Name the blood parasite species.
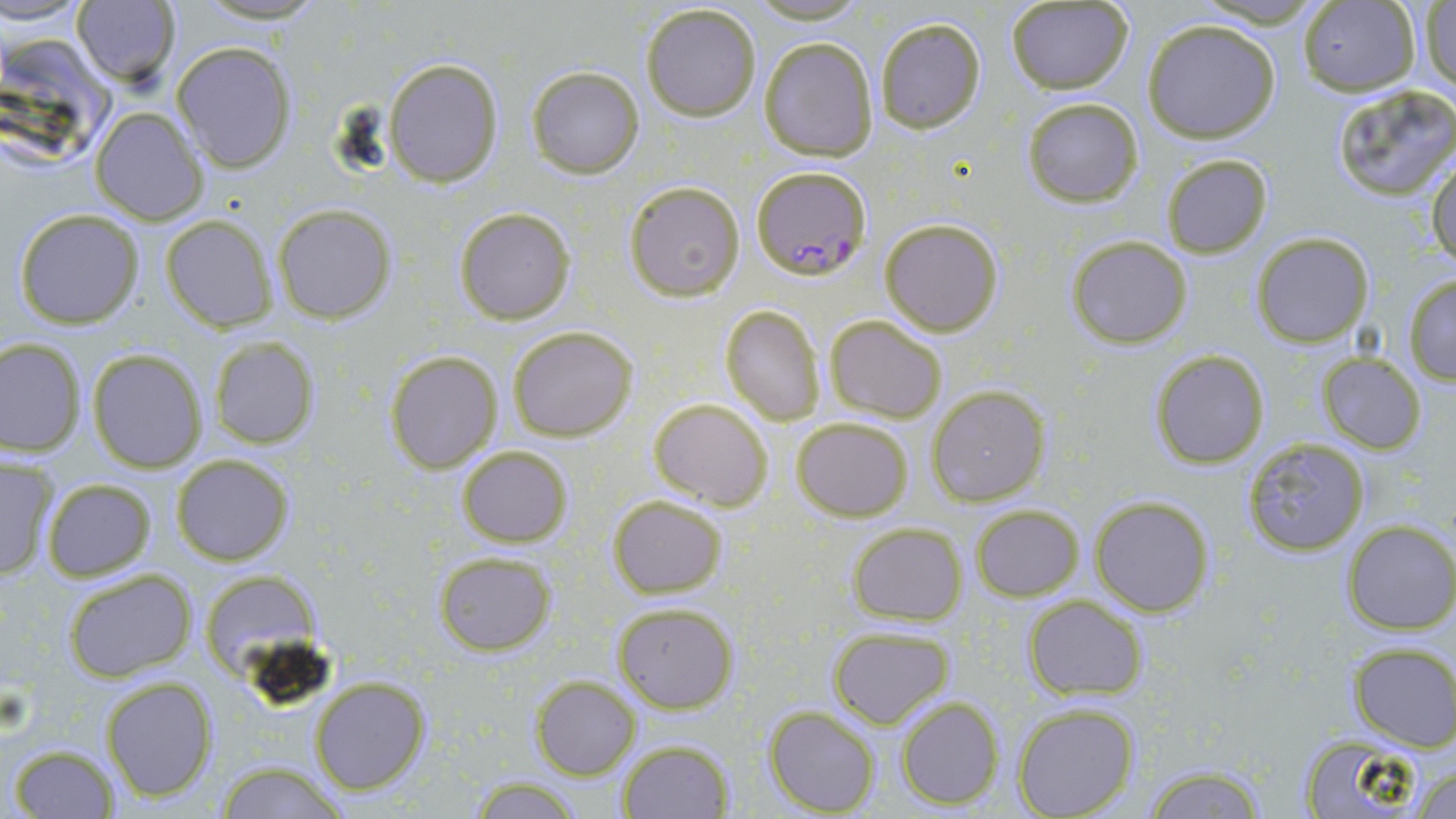
Plasmodium falciparum.

image_size: 1456×819 pixels
plasmodium_falciparum_infected_red_blood_cell_locations: 'approximate bounding boxes as named x1/y1/x2/y2 corners in pixels: (x1=749, y1=166, x2=870, y2=280)'
magnification: 1000x
preparation: thin blood smear
field_of_view: single
uninfected_red_blood_cell_locations: 'approximate bounding boxes as named x1/y1/x2/y2 corners in pixels: (x1=2, y1=0, x2=91, y2=29), (x1=186, y1=0, x2=338, y2=25), (x1=71, y1=1, x2=180, y2=87), (x1=1004, y1=1, x2=1134, y2=95), (x1=1296, y1=1, x2=1420, y2=95), (x1=1419, y1=3, x2=1456, y2=94), (x1=639, y1=4, x2=762, y2=120), (x1=875, y1=17, x2=988, y2=133), (x1=1142, y1=19, x2=1280, y2=144), (x1=0, y1=33, x2=118, y2=175), (x1=760, y1=37, x2=878, y2=163), (x1=170, y1=41, x2=297, y2=173), (x1=384, y1=57, x2=504, y2=186), (x1=526, y1=65, x2=645, y2=179), (x1=1329, y1=84, x2=1456, y2=202), (x1=1021, y1=98, x2=1142, y2=207), (x1=91, y1=107, x2=209, y2=225), (x1=1160, y1=154, x2=1273, y2=259), (x1=1430, y1=155, x2=1455, y2=270), (x1=623, y1=181, x2=745, y2=300), (x1=272, y1=204, x2=396, y2=324), (x1=453, y1=205, x2=576, y2=325), (x1=13, y1=207, x2=145, y2=330), (x1=161, y1=214, x2=278, y2=332), (x1=879, y1=217, x2=1004, y2=336), (x1=1252, y1=233, x2=1373, y2=348), (x1=1067, y1=237, x2=1192, y2=350), (x1=1402, y1=274, x2=1456, y2=384), (x1=720, y1=305, x2=825, y2=425), (x1=825, y1=315, x2=947, y2=422), (x1=506, y1=325, x2=638, y2=442), (x1=208, y1=335, x2=319, y2=449), (x1=0, y1=336, x2=86, y2=457), (x1=86, y1=348, x2=209, y2=472), (x1=384, y1=348, x2=503, y2=473), (x1=1148, y1=349, x2=1270, y2=469), (x1=1315, y1=354, x2=1427, y2=453), (x1=927, y1=385, x2=1049, y2=507), (x1=648, y1=398, x2=774, y2=510), (x1=792, y1=416, x2=912, y2=521), (x1=1242, y1=436, x2=1373, y2=558), (x1=458, y1=446, x2=573, y2=546), (x1=172, y1=454, x2=293, y2=566), (x1=0, y1=455, x2=59, y2=581), (x1=42, y1=479, x2=156, y2=580), (x1=1090, y1=494, x2=1214, y2=616), (x1=608, y1=495, x2=727, y2=598), (x1=971, y1=504, x2=1083, y2=601), (x1=1341, y1=520, x2=1456, y2=634), (x1=846, y1=522, x2=967, y2=626), (x1=433, y1=551, x2=556, y2=657), (x1=61, y1=568, x2=197, y2=683), (x1=208, y1=569, x2=320, y2=686), (x1=1022, y1=595, x2=1148, y2=700), (x1=614, y1=602, x2=739, y2=713), (x1=826, y1=626, x2=956, y2=728), (x1=1346, y1=645, x2=1456, y2=751), (x1=100, y1=675, x2=217, y2=802), (x1=530, y1=675, x2=640, y2=780), (x1=308, y1=676, x2=431, y2=796), (x1=896, y1=695, x2=1004, y2=808), (x1=1012, y1=704, x2=1139, y2=819), (x1=766, y1=705, x2=879, y2=816), (x1=1294, y1=733, x2=1433, y2=817), (x1=616, y1=738, x2=734, y2=818), (x1=8, y1=744, x2=119, y2=817), (x1=1412, y1=762, x2=1455, y2=819), (x1=210, y1=763, x2=351, y2=818), (x1=1141, y1=764, x2=1269, y2=819), (x1=465, y1=777, x2=588, y2=817)'
stain: May-Grünwald-Giemsa
modality: light microscopy